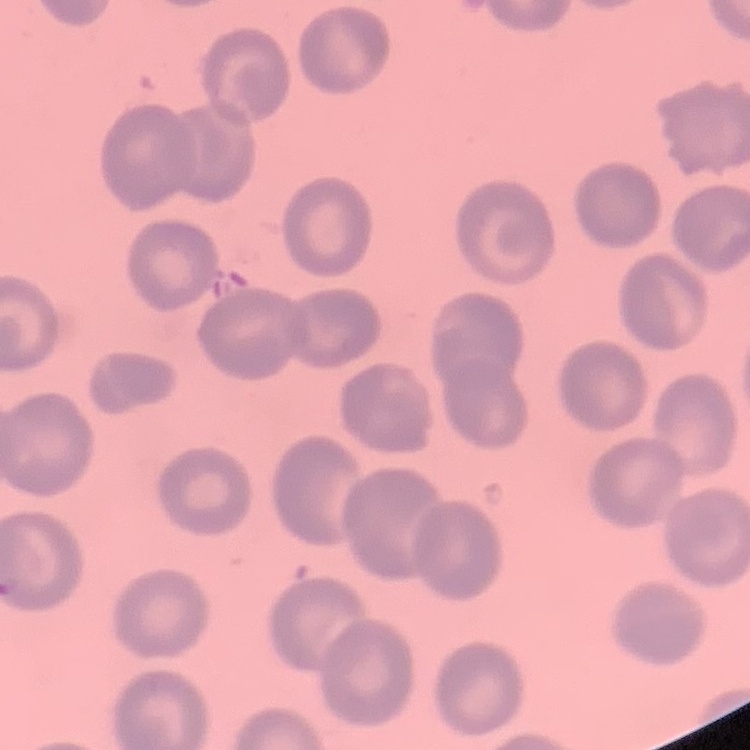

The erythrocytes show no rouleaux formation. Square crop of a larger photomicrograph. Field's or Giemsa stain. Thin blood smear.